Draw a bounding box around every trophozoite.
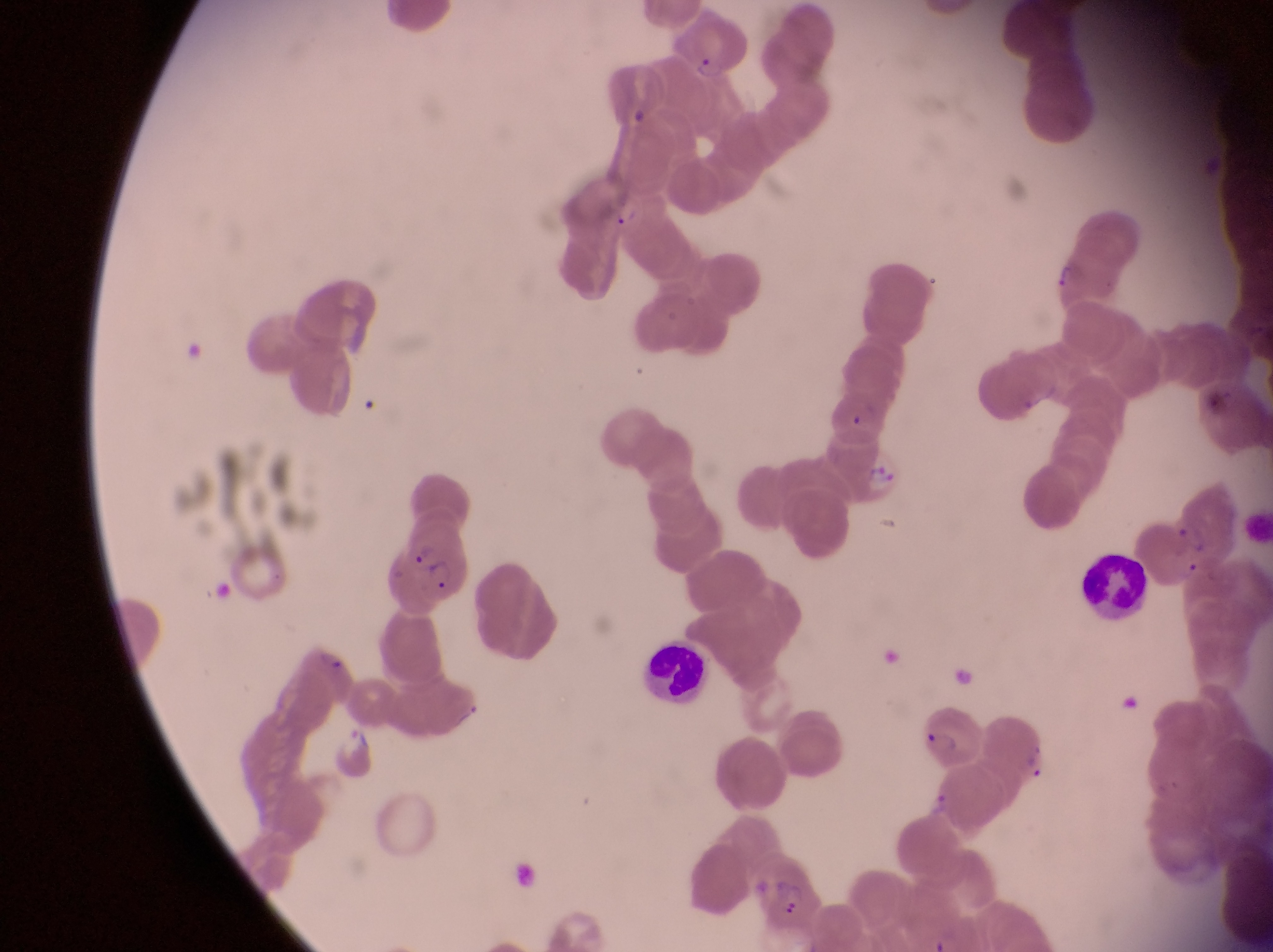
Approximate bounding boxes as (left, top, right, bottom) in pixels.
Trophozoites: (923, 783, 957, 820).

Leukocyte locations: (1077, 547, 1153, 616), (646, 637, 709, 712). Parasitised red blood cell locations: (670, 10, 749, 80), (830, 432, 905, 502), (1163, 475, 1245, 567), (382, 530, 472, 613), (913, 709, 985, 767), (327, 721, 377, 781), (752, 854, 824, 932). Thin blood smear. Captured by a smartphone held over the eyepiece of an Olympus CX-23 microscope. Collected in Uganda. At a magnification of 1000x. One field of view. Image is 1273×952 pixels.